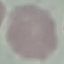

Summary:
  - Malaria status: uninfected
  - Image type: cell patch, automatically extracted from a larger field of view and resized to 64 × 64 pixels
  - Preparation: thin smear
  - Stain: Giemsa
  - Capture: smartphone through the microscope eyepiece